Assess this cell for malaria.
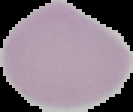

Uninfected.

Summary:
  - Image type: segmented cell region with the area outside set to black
  - Image size: 133×112 pixels
  - Preparation: thin blood smear